Describe the morphology of the erythrocytes.
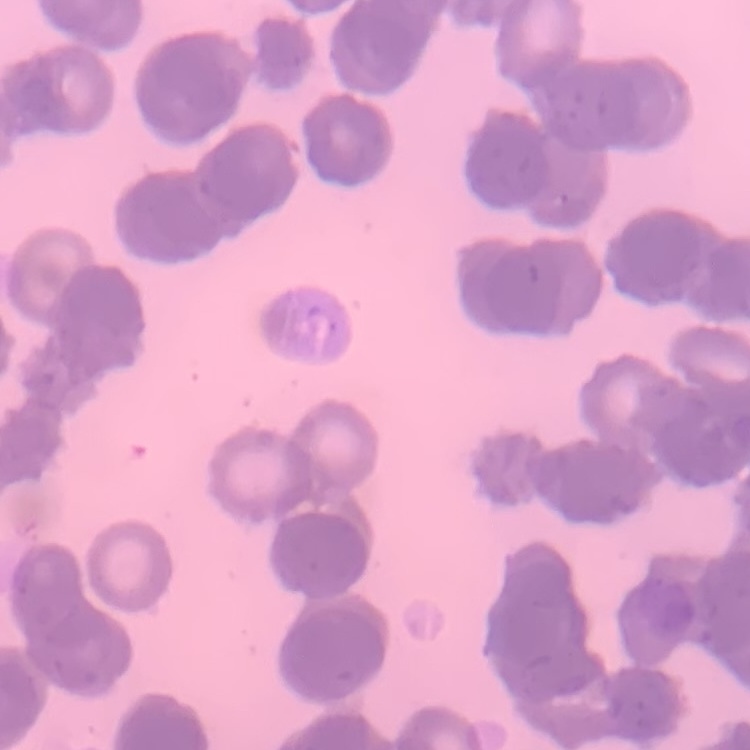

Rouleaux formation.

Summary:
  - Image type: one tile cut from a larger photomicrograph
  - Stain: Field's or Giemsa
  - Preparation: thin peripheral smear